Locate every blood parasite and identify its species.
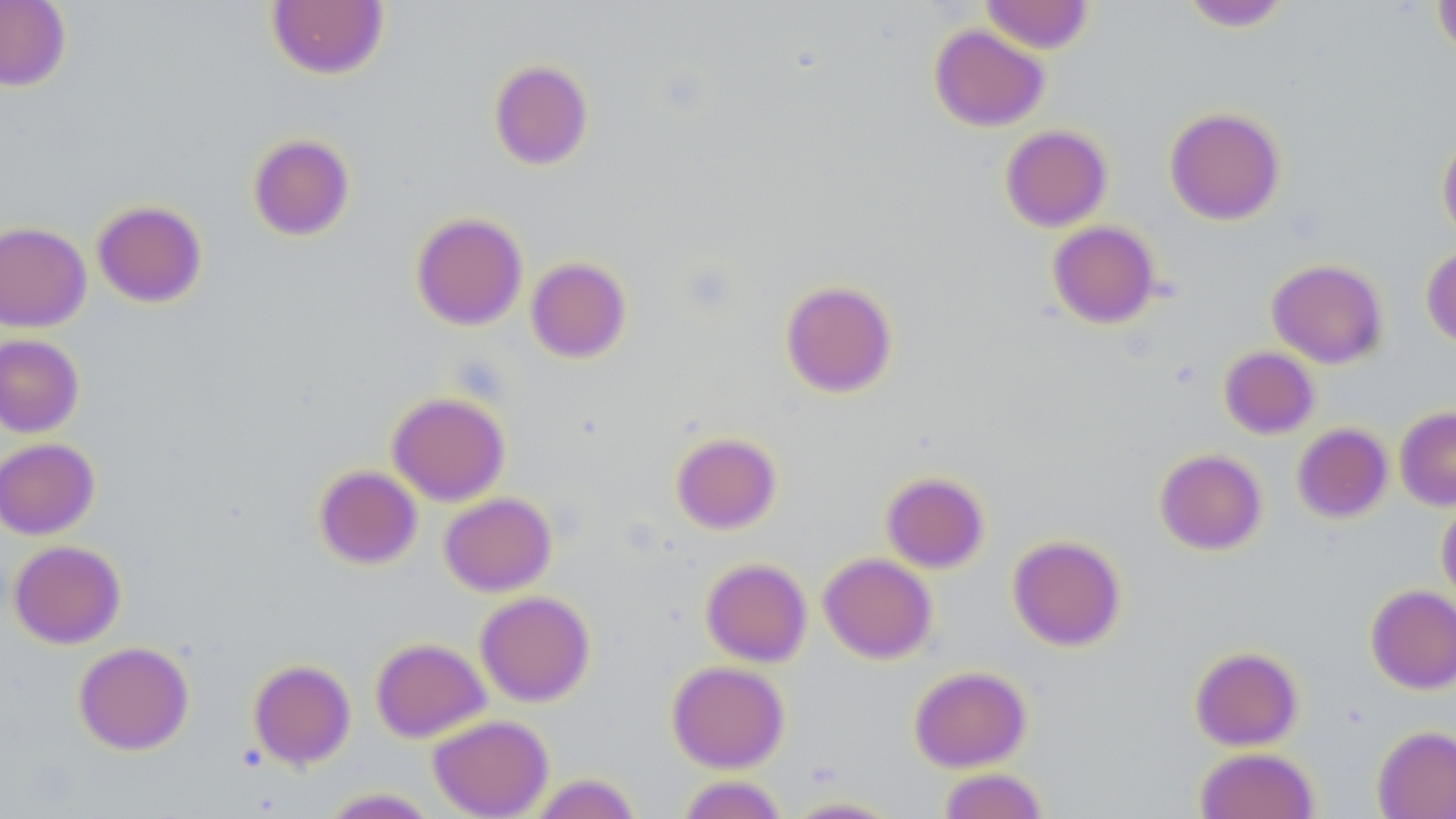

No blood parasites observed.

Approximate bounding boxes as (x1, y1, x2, y2) in pixels. Uninfected red blood cell locations: (0, 0, 71, 91), (1432, 0, 1456, 59), (266, 1, 390, 79), (980, 1, 1094, 54), (1178, 1, 1293, 32), (928, 24, 1050, 131), (488, 59, 593, 170), (1164, 107, 1286, 225), (1000, 124, 1112, 232), (1436, 131, 1456, 246), (247, 133, 355, 241), (91, 200, 207, 308), (411, 212, 527, 330), (1047, 221, 1160, 328), (0, 222, 91, 332), (1421, 246, 1456, 349), (525, 256, 631, 363), (1267, 259, 1388, 368), (780, 279, 897, 397), (0, 334, 84, 438), (1219, 346, 1320, 439), (387, 391, 510, 506), (1394, 406, 1456, 510), (1292, 423, 1393, 523), (671, 431, 781, 534), (0, 437, 100, 540), (1154, 448, 1267, 555), (314, 465, 422, 569), (880, 471, 989, 573), (439, 492, 556, 596), (1436, 496, 1456, 608), (1007, 535, 1126, 651), (8, 540, 126, 648), (818, 552, 937, 664), (700, 557, 812, 667), (1365, 584, 1456, 694), (475, 591, 595, 706), (370, 637, 490, 743), (73, 641, 194, 755), (1189, 646, 1303, 751), (248, 659, 356, 770), (667, 660, 789, 773), (908, 665, 1032, 772), (428, 714, 553, 819), (1372, 725, 1456, 818), (1194, 747, 1319, 819), (938, 767, 1048, 819), (527, 773, 641, 819), (677, 775, 787, 819), (321, 787, 439, 818), (781, 796, 904, 818). Slide-level diagnosis: no evidence of blood parasites. Single field of view. May-Grünwald-Giemsa-stained preparation. 1000x magnification. Image is 1456×819 pixels. Thin blood film. Optical microscopy.